Name the parasite shown.
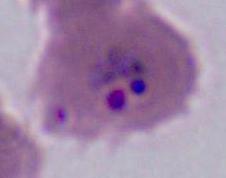

Plasmodium.

modality = micrograph
magnification = 400x or 1000x